Report the malaria status of this cell.
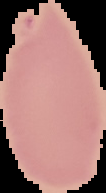
Uninfected.

Summary:
  - Preparation: thin blood film
  - Image type: segmented cell region on a black background
  - Image size: 106×193 pixels